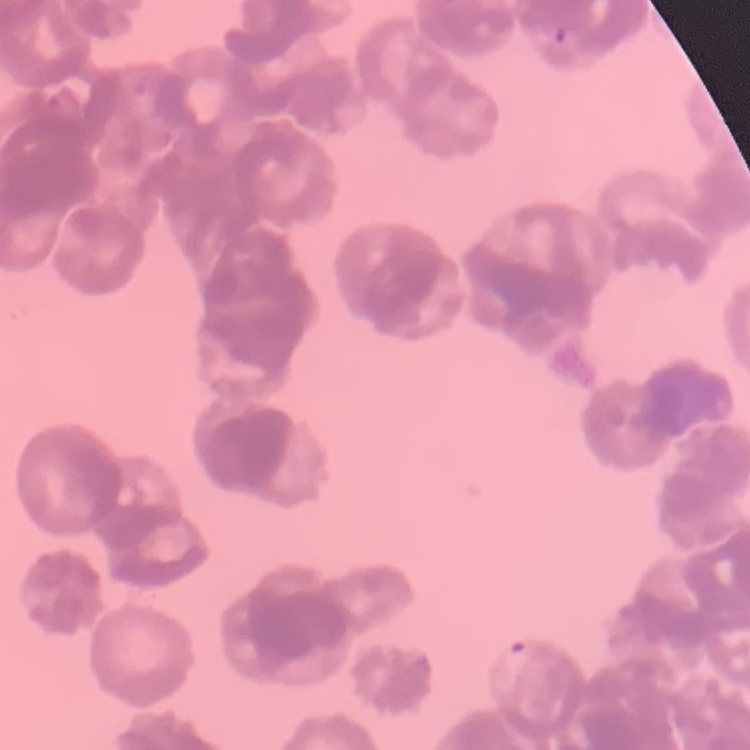
The red blood cells exhibit rouleaux formation. Square crop of a larger photomicrograph. Thin blood smear. Stained with either Field's or Giemsa.